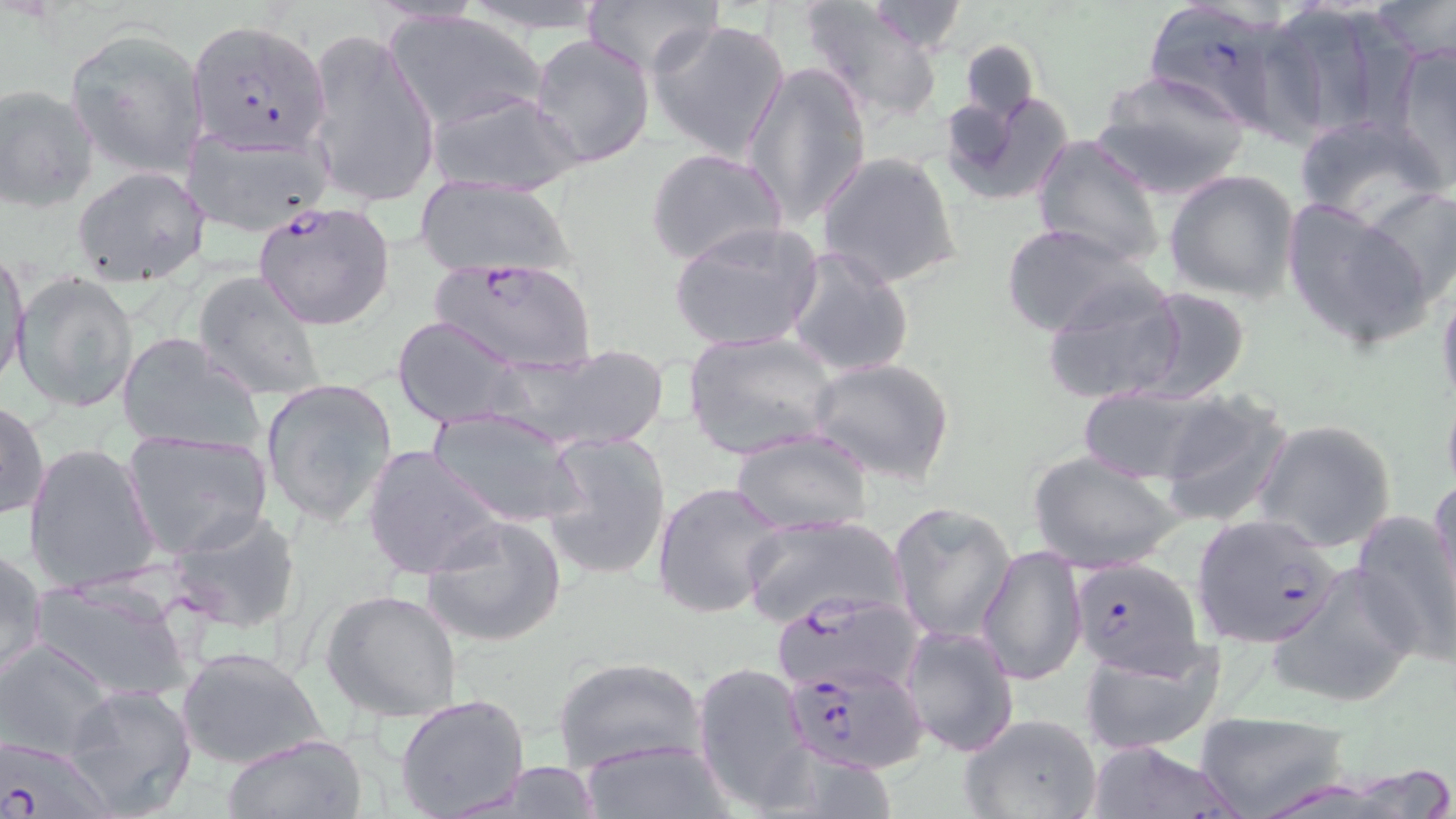
Approximate bounding boxes as (x1, y1, x2, y2) in pixels. Plasmodium falciparum-infected red blood cell locations: (1141, 0, 1304, 132), (186, 19, 332, 154), (250, 198, 396, 331), (429, 256, 597, 375), (1190, 514, 1342, 647), (1070, 557, 1204, 677), (770, 590, 924, 694), (784, 660, 927, 772). Uninfected red blood cell locations: (447, 0, 621, 33), (580, 0, 723, 76), (799, 1, 949, 125), (1373, 1, 1456, 62), (860, 2, 970, 57), (1264, 2, 1403, 141), (384, 9, 548, 133), (650, 18, 791, 162), (65, 28, 209, 180), (301, 29, 440, 208), (527, 33, 655, 169), (959, 37, 1041, 125), (1391, 42, 1456, 185), (744, 61, 873, 229), (1092, 69, 1252, 198), (0, 84, 98, 211), (426, 88, 581, 198), (940, 91, 1076, 207), (1294, 116, 1447, 229), (182, 121, 333, 237), (1031, 134, 1166, 270), (645, 149, 788, 269), (817, 150, 962, 290), (70, 165, 210, 286), (1164, 169, 1300, 303), (414, 176, 575, 277), (1363, 185, 1456, 304), (1280, 198, 1435, 351), (668, 221, 825, 353), (1001, 223, 1155, 339), (785, 245, 915, 379), (1, 248, 30, 390), (191, 270, 327, 402), (14, 271, 139, 415), (1040, 278, 1189, 409), (1437, 280, 1456, 414), (1132, 287, 1252, 405), (391, 317, 526, 427), (683, 329, 840, 460), (117, 333, 262, 456), (495, 343, 669, 453), (807, 356, 955, 485), (260, 379, 398, 529), (1075, 386, 1229, 484), (1441, 389, 1456, 500), (1156, 395, 1294, 526), (0, 399, 49, 520), (430, 407, 585, 529), (1254, 418, 1397, 553), (729, 427, 874, 534), (122, 429, 273, 558), (538, 430, 672, 581), (24, 442, 162, 594), (362, 443, 503, 582), (1029, 449, 1185, 574), (1429, 477, 1456, 608), (652, 481, 791, 619), (888, 501, 1017, 641), (167, 506, 304, 638), (1351, 510, 1456, 665), (420, 514, 567, 647), (740, 516, 907, 627), (976, 545, 1086, 687), (0, 548, 47, 689), (1268, 565, 1421, 710), (31, 578, 195, 705), (321, 590, 463, 723), (898, 623, 1018, 758), (0, 639, 115, 761), (1079, 643, 1226, 757), (176, 645, 331, 771), (550, 654, 709, 772), (692, 660, 813, 812), (62, 683, 199, 818), (394, 693, 531, 819), (1190, 709, 1351, 819), (958, 712, 1101, 819), (222, 733, 368, 819), (1, 737, 113, 817), (577, 737, 731, 819), (1084, 739, 1244, 819), (472, 761, 607, 817). Slide-level diagnosis: Plasmodium falciparum. Thin blood smear. Image is 1456×819 pixels. One field of a larger specimen. 1000x magnification. May-Grünwald-Giemsa stain. Optical microscopy.